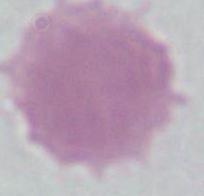
Summary:
  - Modality: micrograph
  - Magnification: 1000x
  - Identification: red blood cell